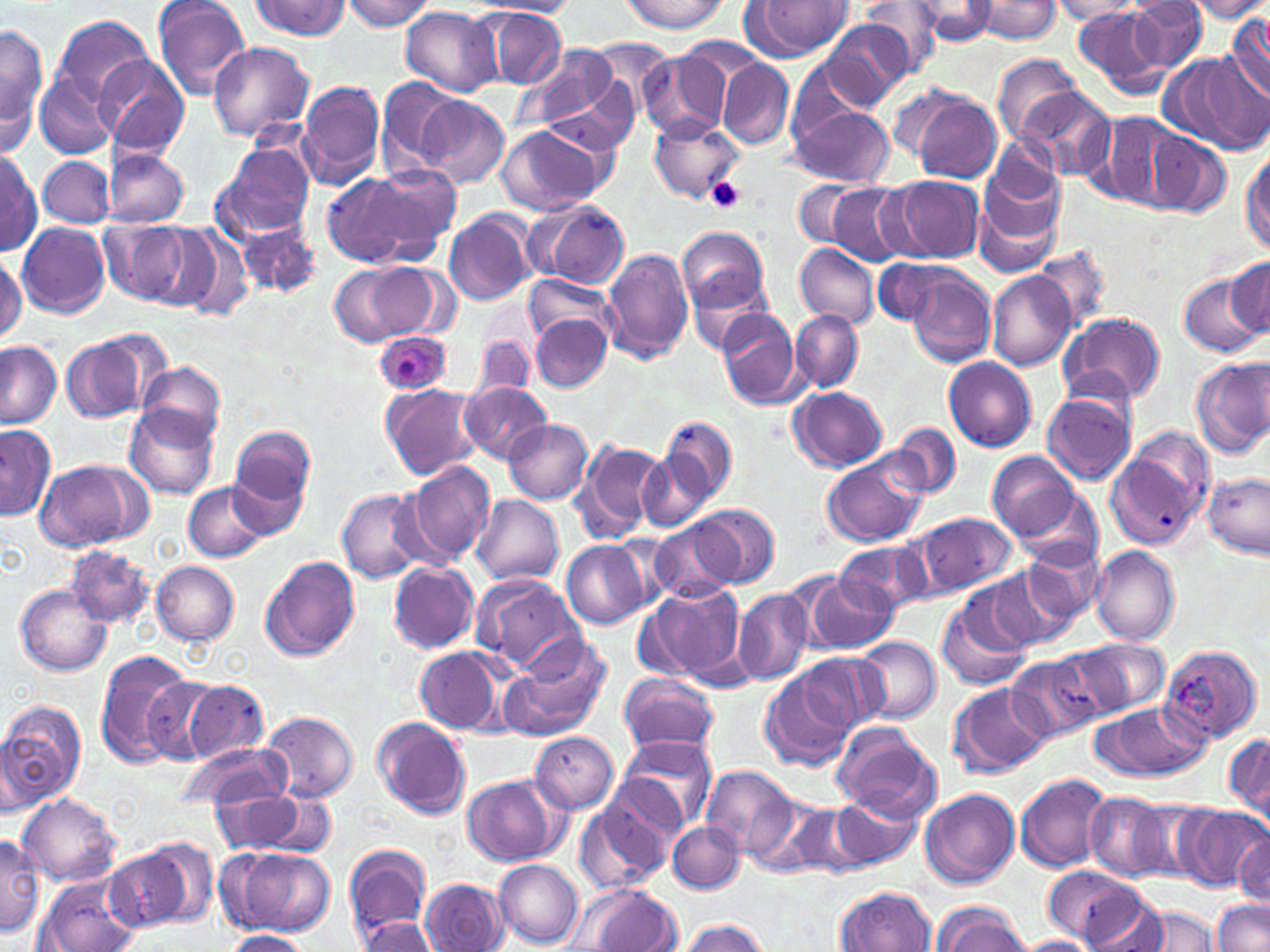 Approximate bounding boxes as (x1,y1)-(x2,y2) corner pairs in pixels. Plasmodium ovale-infected red blood cell locations: (373,329)-(452,396). Platelet locations: (708,177)-(746,213). Uninfected red blood cell locations: (151,0)-(253,100), (340,0)-(436,31), (620,0)-(733,33), (861,0)-(949,74), (971,0)-(1062,43), (1128,0)-(1208,73), (1186,0)-(1270,22), (467,1)-(575,18), (747,1)-(856,59), (1050,1)-(1142,22), (246,2)-(352,41), (910,2)-(1000,45), (1072,6)-(1168,97), (400,7)-(503,98), (485,9)-(567,88), (1227,10)-(1270,103), (49,14)-(153,106), (819,19)-(914,110), (0,23)-(47,150), (586,39)-(676,113), (207,41)-(315,143), (519,46)-(621,137), (1163,51)-(1264,153), (640,52)-(727,139), (95,55)-(190,159), (994,56)-(1084,143), (717,57)-(794,151), (787,58)-(876,148), (34,68)-(120,161), (374,79)-(463,172), (296,80)-(386,191), (887,83)-(967,165), (1014,87)-(1115,184), (413,91)-(510,189), (911,93)-(1004,184), (787,102)-(895,188), (1092,110)-(1188,209), (650,115)-(743,202), (495,124)-(604,216), (1145,129)-(1231,216), (211,144)-(315,243), (1241,145)-(1270,256), (1,147)-(42,255), (102,150)-(189,228), (38,155)-(114,227), (975,157)-(1069,272), (367,163)-(462,256), (321,172)-(425,268), (886,176)-(986,263), (794,180)-(871,249), (825,183)-(912,266), (533,200)-(629,289), (444,209)-(536,306), (232,217)-(320,299), (98,219)-(193,307), (155,221)-(253,319), (18,222)-(111,318), (676,226)-(770,314), (793,242)-(880,329), (0,247)-(26,346), (602,248)-(694,365), (1034,249)-(1112,330), (871,256)-(952,326), (1219,256)-(1270,344), (329,261)-(433,348), (905,268)-(997,366), (987,270)-(1078,372), (1179,270)-(1264,357), (686,273)-(776,353), (524,274)-(616,348), (716,309)-(804,410), (790,310)-(864,394), (1059,311)-(1166,405), (531,316)-(613,391), (471,331)-(537,402), (61,332)-(157,424), (0,342)-(61,430), (944,357)-(1037,452), (1191,357)-(1270,459), (138,360)-(227,445), (460,381)-(551,463), (380,383)-(482,481), (790,387)-(888,471), (1042,390)-(1137,484), (124,404)-(218,499), (662,413)-(738,507), (503,419)-(593,504), (890,422)-(961,499), (1,424)-(57,520), (230,425)-(316,522), (1102,432)-(1206,546), (574,438)-(663,544), (638,450)-(711,530), (821,450)-(930,548), (987,451)-(1081,541), (35,457)-(154,551), (406,461)-(496,564), (1202,472)-(1268,556), (184,480)-(270,563), (1012,483)-(1104,571), (337,488)-(428,583), (472,495)-(564,585), (692,504)-(779,588), (907,510)-(1018,601), (654,519)-(740,602), (562,540)-(651,628), (835,540)-(930,618), (1022,543)-(1105,624), (1090,545)-(1180,644), (64,546)-(153,628), (259,556)-(361,663), (151,561)-(240,645), (389,562)-(478,654), (987,564)-(1082,651), (471,572)-(582,672), (801,572)-(895,654), (641,582)-(747,686), (15,584)-(113,676), (734,586)-(813,686), (936,596)-(1033,692), (853,635)-(941,724), (1061,636)-(1170,721), (500,640)-(609,740), (1161,643)-(1263,743), (415,647)-(506,733), (94,651)-(198,769), (1005,651)-(1105,744), (796,652)-(888,733), (759,670)-(858,772), (617,672)-(721,755), (143,676)-(224,764), (180,679)-(268,763), (950,683)-(1050,778), (0,699)-(86,808), (1095,701)-(1209,781), (259,711)-(357,801), (372,718)-(470,819), (832,722)-(940,820), (530,730)-(620,813), (1222,730)-(1269,827), (620,734)-(719,830), (178,742)-(287,813), (702,764)-(800,863), (601,772)-(686,857), (1015,773)-(1111,873), (461,774)-(564,867), (211,787)-(327,857), (921,787)-(1020,888), (1085,791)-(1177,881), (830,792)-(922,871), (18,793)-(120,885), (765,796)-(859,879), (575,799)-(672,895), (1177,806)-(1265,889), (667,821)-(745,894), (1232,831)-(1268,905), (0,832)-(43,936), (139,839)-(218,926), (344,843)-(433,939), (220,845)-(335,938), (105,848)-(193,935), (494,859)-(584,947), (1042,865)-(1152,945), (37,876)-(138,952), (421,878)-(509,952), (570,884)-(682,951), (836,885)-(938,952), (1077,891)-(1170,952), (1212,899)-(1270,951), (933,903)-(1030,952), (1131,904)-(1220,950), (358,916)-(436,951), (677,919)-(772,952), (221,929)-(310,952), (1016,936)-(1104,952). Slide-level diagnosis: Plasmodium ovale. 1000x magnification. One field of a larger specimen. Image is 1270×952 pixels. Thin blood film. Optical microscopy. May-Grünwald-Giemsa-stained preparation.